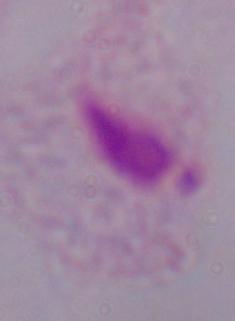
Photomicrograph. Captured at 1000x magnification. A trichomonad is seen.